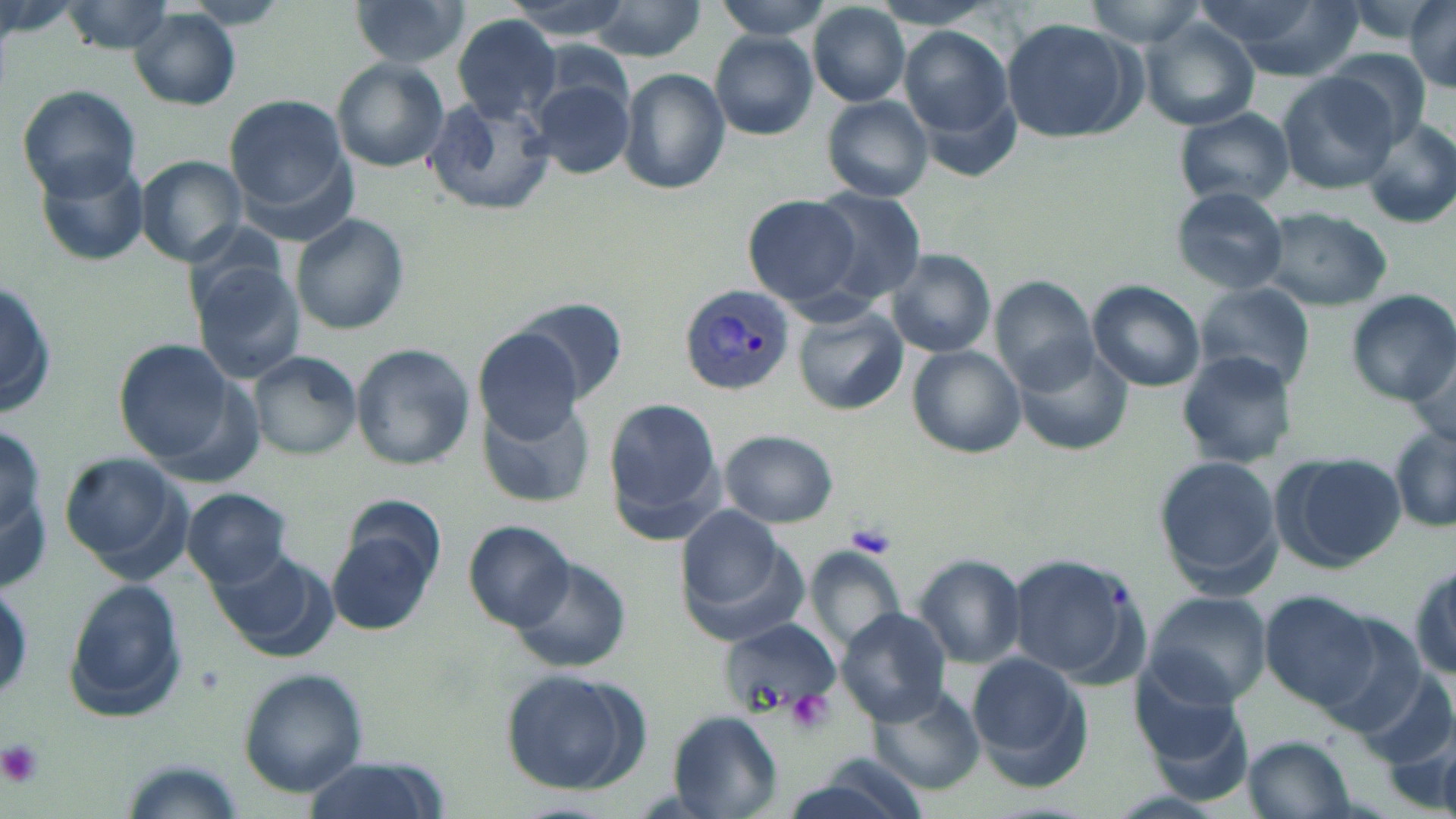
Summary:
  - Coordinate format: approximate bounding boxes as (x1,y1)-(x2,y2) corner pairs in pixels
  - Uninfected red blood cell locations: (346,0)-(472,68), (503,0)-(634,39), (714,0)-(837,40), (868,0)-(1002,31), (1082,0)-(1209,47), (1196,0)-(1363,77), (1408,0)-(1456,93), (583,1)-(708,60), (184,2)-(291,30), (62,3)-(180,53), (808,4)-(910,107), (129,9)-(241,110), (451,14)-(562,125), (1001,18)-(1140,141), (1141,20)-(1259,129), (898,28)-(1015,152), (711,34)-(818,139), (1326,48)-(1435,143), (332,59)-(450,171), (619,67)-(731,196), (1278,74)-(1398,193), (531,75)-(635,178), (16,83)-(140,198), (226,95)-(353,218), (822,95)-(934,202), (424,97)-(556,215), (1174,108)-(1295,207), (1361,114)-(1456,226), (31,153)-(151,268), (136,156)-(248,267), (1169,186)-(1289,296), (805,187)-(927,304), (743,196)-(864,308), (1260,207)-(1393,309), (292,214)-(409,334), (885,249)-(996,357), (190,261)-(304,382), (0,273)-(57,423), (991,279)-(1101,393), (1089,282)-(1205,393), (1195,283)-(1314,394), (1342,290)-(1456,405), (506,297)-(626,407), (793,302)-(908,414), (473,327)-(589,443), (116,339)-(234,462), (1015,340)-(1129,453), (351,344)-(475,469), (908,346)-(1027,458), (247,350)-(362,461), (1176,350)-(1299,468), (481,397)-(593,509), (606,397)-(725,539), (0,413)-(51,581), (1389,425)-(1456,534), (719,430)-(839,528), (60,450)-(188,573), (1273,452)-(1405,572), (1155,456)-(1282,588), (183,489)-(292,587), (677,510)-(807,646), (328,513)-(440,633), (465,520)-(574,633), (209,543)-(335,659), (808,545)-(906,654), (1009,551)-(1143,682), (917,553)-(1026,668), (1409,554)-(1456,681), (511,555)-(634,672), (62,579)-(187,723), (1264,590)-(1380,709), (1146,593)-(1271,706), (838,608)-(951,726), (1315,615)-(1427,735), (722,619)-(838,718), (969,652)-(1095,788), (1130,658)-(1253,779), (236,669)-(368,795), (498,669)-(651,794), (1361,671)-(1452,772), (868,684)-(985,796), (666,709)-(783,817), (1243,735)-(1356,819), (297,757)-(445,819), (763,767)-(926,819)
  - Plasmodium vivax-infected red blood cell locations: (681,286)-(794,397)
  - Platelet locations: (846,523)-(896,558), (787,689)-(832,733), (0,738)-(44,790)
  - Slide-level diagnosis: Plasmodium vivax
  - Image size: 1456×819 pixels
  - Stain: May-Grünwald-Giemsa
  - Field of view: single
  - Preparation: thin blood film
  - Magnification: 1000x
  - Modality: optical microscopy